State which parasite is depicted.
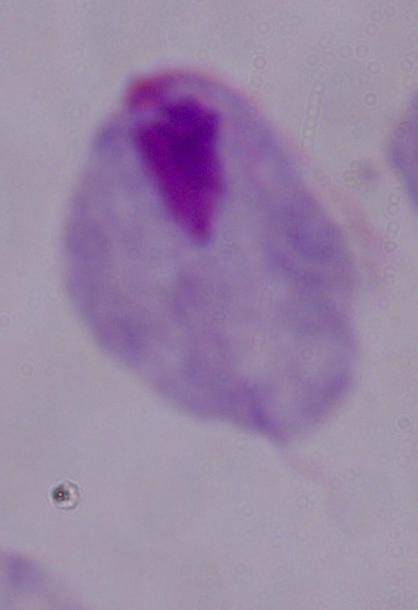
A trichomonad.

Summary:
  - Magnification: 1000x
  - Modality: micrograph